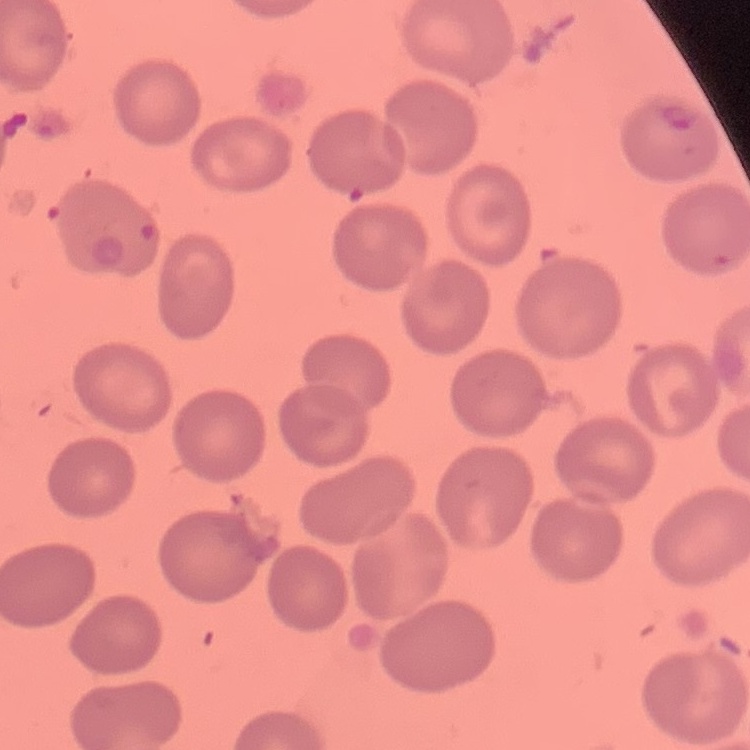

Summary:
  - Red blood cell morphology: no rouleaux formation
  - Stain: Field's or Giemsa
  - Image type: square crop of a larger photomicrograph
  - Preparation: thin blood film